Give the position of every malaria parasite.
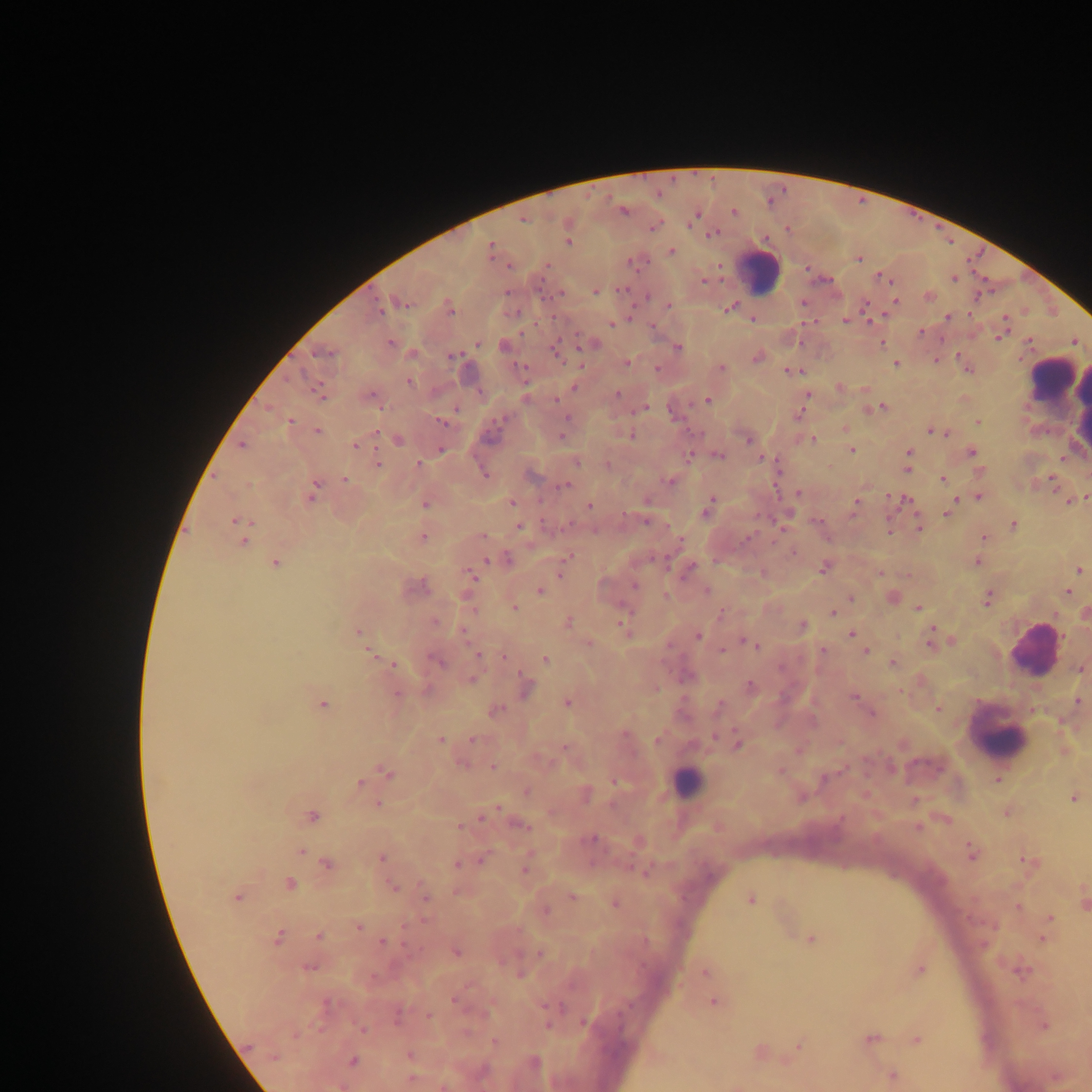

Approximate centers as {x, y} in pixels.
Malaria parasites: {658, 193}, {768, 201}, {732, 210}, {623, 213}, {699, 215}, {655, 227}, {650, 228}, {787, 229}, {715, 233}, {709, 234}, {489, 243}, {672, 251}, {858, 259}, {630, 263}, {719, 264}, {549, 265}, {807, 269}, {877, 276}, {953, 279}, {704, 281}, {889, 281}, {621, 289}, {595, 291}, {648, 297}, {895, 300}, {404, 303}, {670, 305}, {734, 305}, {862, 305}, {728, 309}, {381, 310}, {970, 314}, {552, 317}, {752, 318}, {947, 318}, {1005, 318}, {845, 321}, {869, 323}, {612, 324}, {653, 324}, {521, 331}, {922, 332}, {998, 339}, {390, 342}, {1030, 342}, {556, 343}, {478, 345}, {883, 345}, {677, 346}, {315, 353}, {330, 353}, {958, 354}, {758, 356}, {936, 359}, {627, 363}, {897, 363}, {720, 365}, {658, 368}, {968, 370}, {787, 371}, {288, 379}, {409, 380}, {840, 387}, {618, 393}, {809, 393}, {555, 400}, {708, 400}, {690, 405}, {267, 406}, {884, 406}, {645, 407}, {455, 409}, {638, 409}, {630, 413}, {504, 418}, {291, 420}, {978, 420}, {443, 424}, {844, 428}, {929, 430}, {318, 431}, {946, 432}, {376, 433}, {631, 434}, {562, 435}, {814, 439}, {398, 441}, {748, 441}, {240, 445}, {354, 445}, {440, 448}, {853, 449}, {909, 451}, {972, 452}, {721, 455}, {690, 456}, {1060, 457}, {760, 458}, {378, 463}, {417, 463}, {608, 464}, {907, 469}, {485, 474}, {1050, 476}, {942, 479}, {345, 480}, {671, 481}, {249, 485}, {316, 485}, {569, 485}, {558, 487}, {1085, 495}, {309, 496}, {888, 496}, {980, 497}, {907, 498}, {713, 499}, {957, 500}, {1069, 500}, {511, 501}, {855, 501}, {426, 504}, {589, 507}, {705, 513}, {853, 514}, {892, 514}, {624, 515}, {946, 515}, {758, 516}, {917, 516}, {234, 520}, {645, 522}, {1014, 525}, {519, 527}, {780, 528}, {919, 529}, {890, 531}, {483, 535}, {747, 536}, {423, 537}, {985, 537}, {680, 540}, {243, 541}, {772, 542}, {794, 552}, {567, 556}, {507, 558}, {486, 560}, {978, 561}, {275, 563}, {823, 567}, {1080, 570}, {880, 572}, {560, 575}, {471, 576}, {634, 585}, {540, 591}, {1068, 591}, {850, 597}, {987, 601}, {515, 608}, {629, 608}, {917, 609}, {832, 612}, {720, 613}, {1055, 615}, {435, 622}, {568, 622}, {620, 624}, {803, 625}, {932, 628}, {358, 631}, {463, 632}, {851, 633}, {932, 636}, {699, 637}, {741, 638}, {951, 640}, {745, 643}, {589, 644}, {929, 646}, {757, 647}, {721, 650}, {822, 650}, {369, 651}, {866, 651}, {480, 654}, {504, 657}, {545, 659}, {438, 661}, {892, 662}, {392, 664}, {521, 673}, {471, 677}, {750, 686}, {899, 692}, {854, 696}, {566, 702}, {322, 704}, {497, 708}, {938, 708}, {872, 713}, {734, 729}, {625, 736}, {712, 736}, {471, 739}, {441, 740}, {658, 741}, {737, 745}, {564, 747}, {551, 761}, {461, 762}, {493, 767}, {385, 772}, {998, 780}, {615, 781}, {361, 783}, {525, 791}, {1073, 798}, {378, 803}, {497, 808}, {310, 815}, {480, 818}, {459, 826}, {529, 827}, {917, 828}, {593, 838}, {301, 850}, {382, 857}, {1019, 858}, {480, 861}, {474, 863}, {456, 864}, {327, 865}, {629, 865}, {524, 870}, {290, 883}, {393, 887}, {426, 896}, {570, 896}, {239, 897}, {1083, 897}, {752, 899}, {545, 910}, {1049, 917}, {424, 919}, {358, 927}, {279, 935}, {319, 935}, {811, 938}, {1040, 938}, {383, 940}, {406, 946}, {457, 951}, {539, 952}, {308, 965}, {706, 972}, {520, 973}, {469, 985}, {454, 1000}, {713, 1002}, {327, 1004}, {543, 1007}, {428, 1014}, {581, 1021}, {547, 1025}, {1043, 1025}, {362, 1030}, {915, 1041}, {495, 1042}, {798, 1044}, {248, 1046}, {409, 1055}, {274, 1057}, {353, 1059}.

Leukocyte locations: {761, 267}, {1053, 374}, {1032, 647}, {998, 733}, {688, 780}. Thick blood film. Sample from Ghana. Mobile-phone photograph taken through the microscope. Image is 1092×1092 pixels. Single field of view.